Locate and identify every blood parasite.
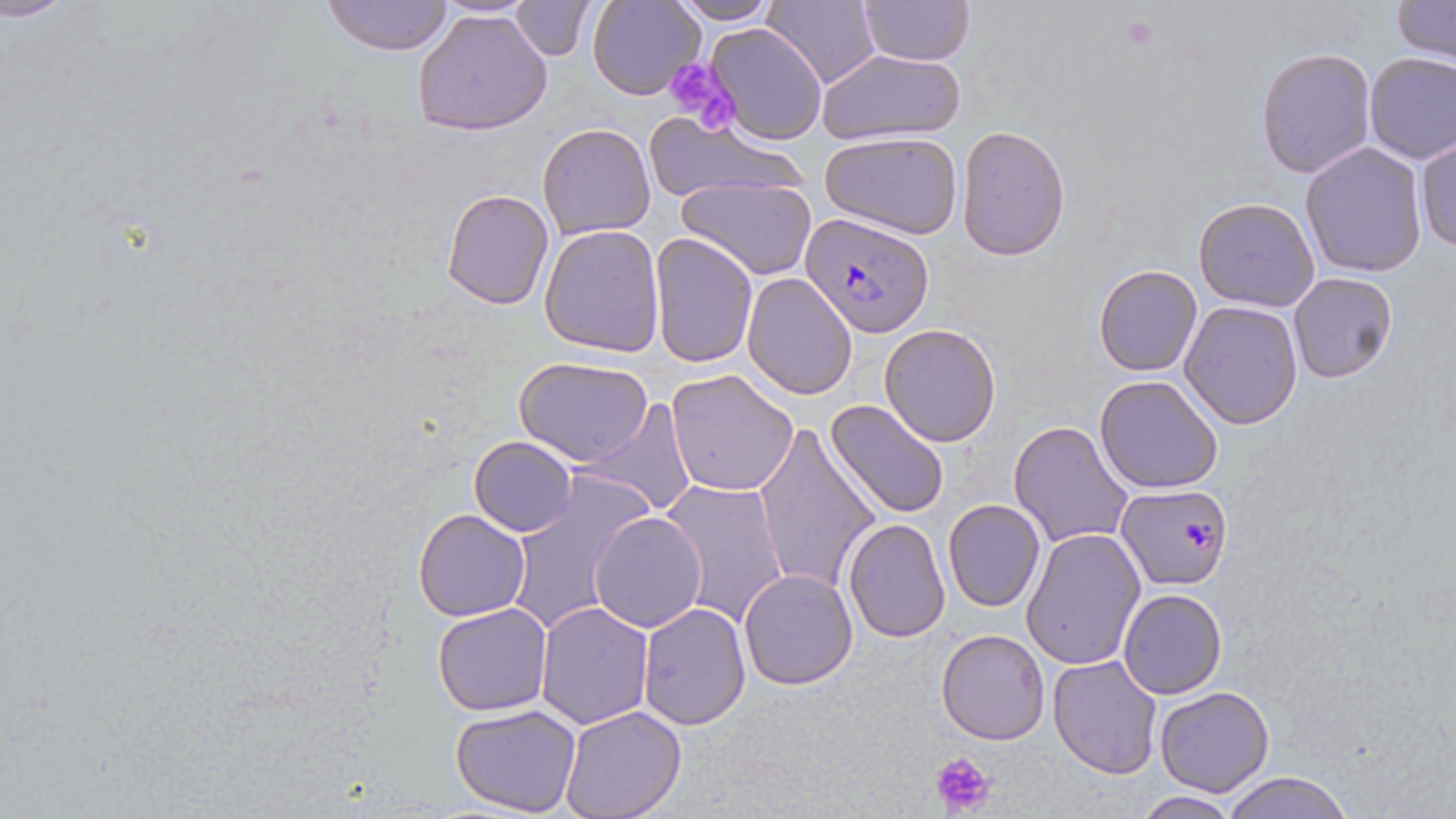

Approximate bounding boxes as [x1, y1, x2, y2] in pixels.
Plasmodium falciparum-infected red blood cells: [801, 212, 934, 336], [1114, 482, 1233, 588].
No Plasmodium ovale, Plasmodium malariae, Plasmodium vivax, Babesia divergens, or Trypanosoma brucei observed.

Uninfected red blood cell locations: [1, 0, 73, 23], [323, 0, 454, 55], [510, 0, 597, 60], [667, 0, 781, 24], [586, 1, 705, 101], [761, 1, 881, 89], [856, 1, 976, 65], [1391, 1, 1454, 62], [412, 7, 553, 136], [703, 22, 828, 145], [1256, 47, 1377, 179], [817, 49, 965, 146], [1363, 52, 1456, 163], [641, 113, 812, 206], [538, 123, 655, 240], [956, 125, 1070, 262], [820, 131, 964, 238], [1413, 137, 1456, 254], [1300, 143, 1429, 278], [678, 176, 815, 278], [441, 188, 555, 310], [1193, 197, 1320, 312], [539, 223, 666, 358], [646, 232, 758, 371], [1093, 264, 1202, 377], [740, 272, 858, 400], [1288, 272, 1397, 384], [1180, 299, 1303, 430], [878, 323, 1002, 447], [514, 356, 652, 467], [666, 367, 800, 498], [1094, 374, 1223, 494], [583, 398, 697, 517], [824, 399, 950, 520], [1010, 421, 1133, 549], [753, 424, 880, 594], [469, 436, 576, 537], [502, 473, 653, 635], [659, 479, 791, 626], [942, 499, 1045, 614], [412, 509, 530, 622], [590, 510, 707, 631], [841, 518, 951, 644], [1021, 528, 1147, 672], [736, 568, 858, 691], [1117, 588, 1226, 699], [534, 602, 654, 727], [431, 603, 553, 715], [638, 604, 751, 728], [935, 629, 1051, 746], [1047, 654, 1162, 777], [1153, 686, 1273, 797], [450, 704, 583, 818], [558, 705, 687, 819], [1224, 771, 1351, 819], [1134, 792, 1240, 818]. Platelet locations: [1117, 15, 1160, 50], [659, 56, 739, 135], [931, 750, 997, 818]. Slide-level diagnosis: Plasmodium falciparum. Thin blood film. One field of a larger specimen. 1000x magnification. Light microscopy. Image is 1456×819 pixels. May-Grünwald-Giemsa stain.